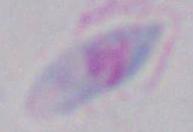

Summary:
  - Identification: Toxoplasma gondii
  - Modality: photomicrograph
  - Magnification: 1000x